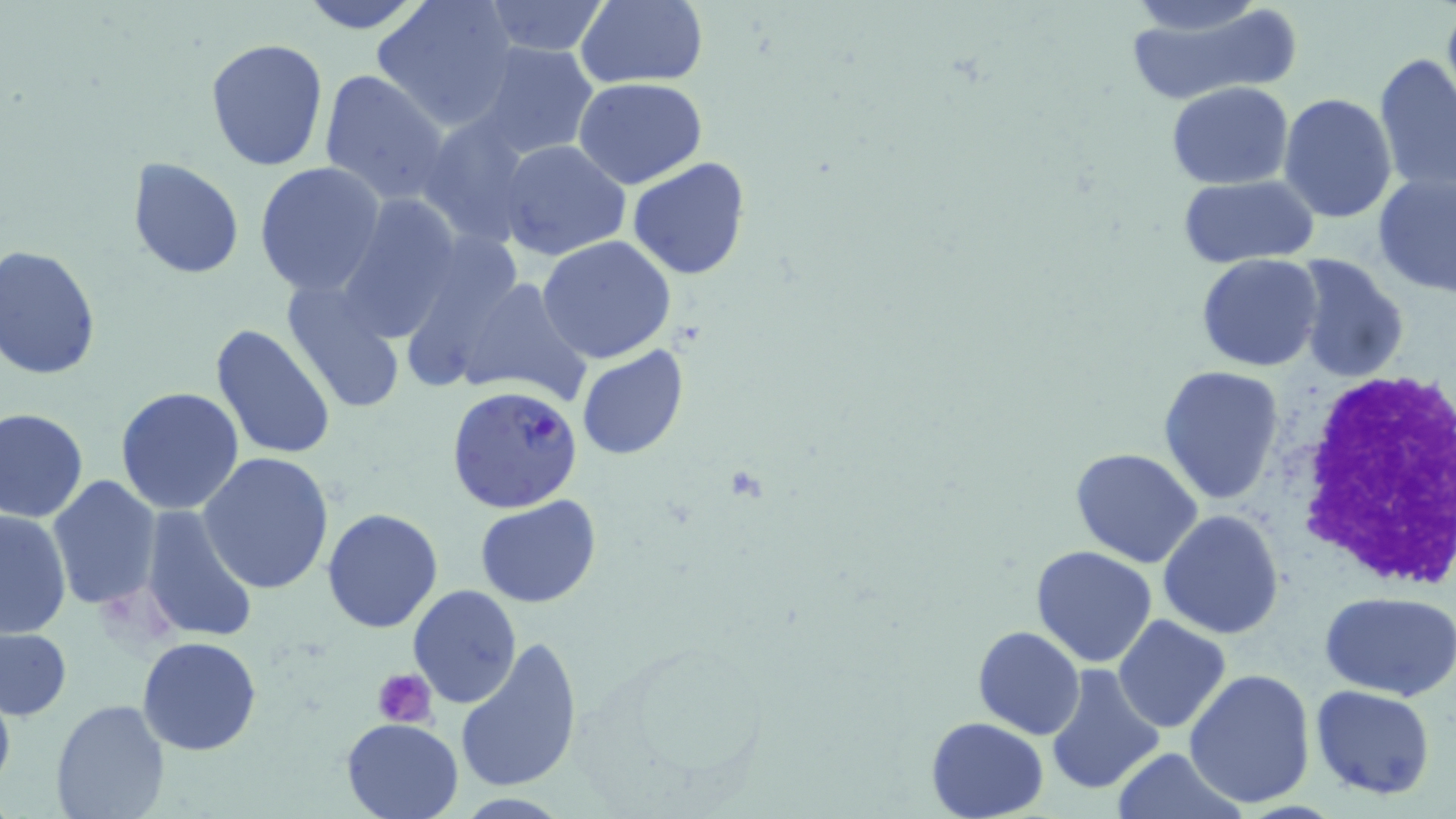
Summary:
  - Coordinate format: approximate bounding boxes as (x1,y1)-(x2,y2) corner pairs in pixels
  - White blood cell locations: (1282,360)-(1452,592)
  - Uninfected red blood cell locations: (299,0)-(430,33), (372,0)-(518,129), (1122,0)-(1293,105), (1125,0)-(1270,40), (480,1)-(611,56), (574,1)-(708,89), (1442,4)-(1456,100), (205,39)-(331,173), (472,40)-(602,160), (1374,53)-(1456,193), (318,69)-(452,206), (574,77)-(707,188), (1167,82)-(1294,187), (1280,93)-(1397,224), (418,112)-(537,244), (498,139)-(632,262), (627,157)-(749,281), (127,158)-(246,278), (254,162)-(387,297), (1372,170)-(1456,297), (1178,176)-(1322,267), (336,194)-(463,341), (537,235)-(676,364), (0,244)-(101,381), (1196,253)-(1324,372), (1289,254)-(1410,383), (441,274)-(592,409), (281,281)-(407,414), (210,324)-(338,461), (576,345)-(688,461), (1159,365)-(1285,506), (114,387)-(245,516), (1,407)-(89,523), (1070,446)-(1203,568), (197,453)-(337,596), (46,474)-(162,614), (475,495)-(600,607), (138,502)-(260,646), (321,507)-(446,632), (0,509)-(72,638), (1158,509)-(1285,640), (1030,545)-(1160,668), (408,585)-(523,710), (1319,590)-(1456,700), (1113,614)-(1231,733), (0,626)-(72,722), (972,626)-(1085,740), (454,634)-(584,795), (137,637)-(264,756), (1043,663)-(1165,798), (1183,669)-(1316,810), (0,682)-(16,800), (1311,685)-(1436,800), (49,699)-(171,819), (925,715)-(1050,819), (340,717)-(465,818), (1113,747)-(1241,819)
  - Platelet locations: (375,668)-(436,728)
  - Plasmodium falciparum-infected red blood cell locations: (447,384)-(587,514)
  - Slide-level diagnosis: Plasmodium falciparum
  - Stain: May-Grünwald-Giemsa
  - Image size: 1456×819 pixels
  - Field of view: single
  - Magnification: 1000x
  - Modality: light microscopy
  - Preparation: thin blood film